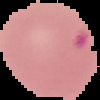
{
  "image_type": "segmented cell region with the area outside set to black",
  "malaria_status": "parasitized",
  "preparation": "thin blood smear",
  "image_size": "100×100 pixels"
}